Assess the morphology of the red blood cells.
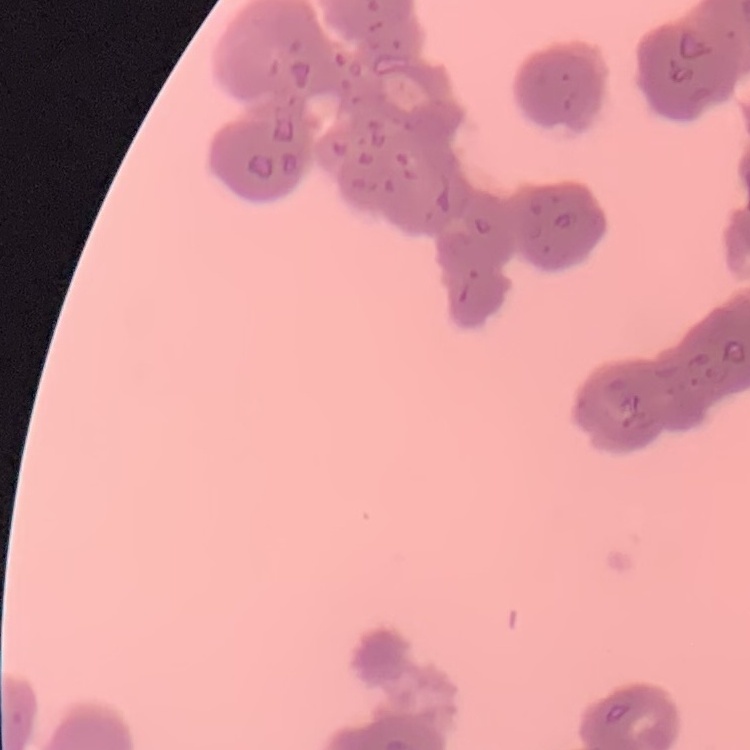
They show rouleaux formation.

Thin blood film. Square crop of a larger photomicrograph. Stained with either Field's or Giemsa.